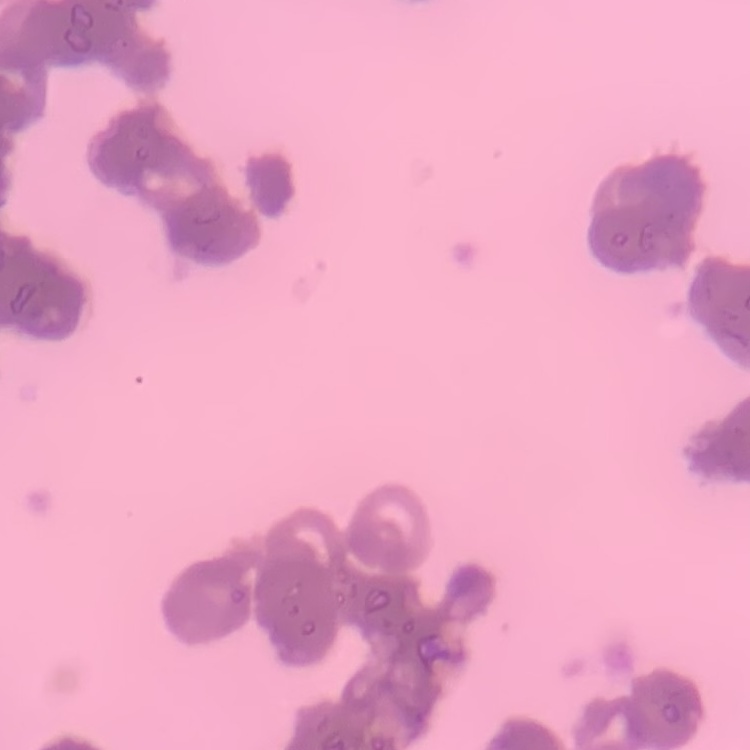

red blood cell morphology = rouleaux formation
stain = Field's or Giemsa
image type = square crop of a larger photomicrograph
preparation = thin peripheral smear